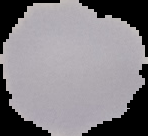
Summary:
  - Image type: segmented cell region on a black background
  - Preparation: thin blood smear
  - Image size: 148×136 pixels
  - Result: no Plasmodium parasites detected